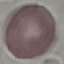 Result: no malaria parasites detected. Giemsa-stained preparation. Cell patch, automatically extracted from a larger field of view and resized to 64 × 64 pixels. Thin blood film. Photographed with a smartphone camera at the microscope eyepiece.